Point out each Plasmodium parasite.
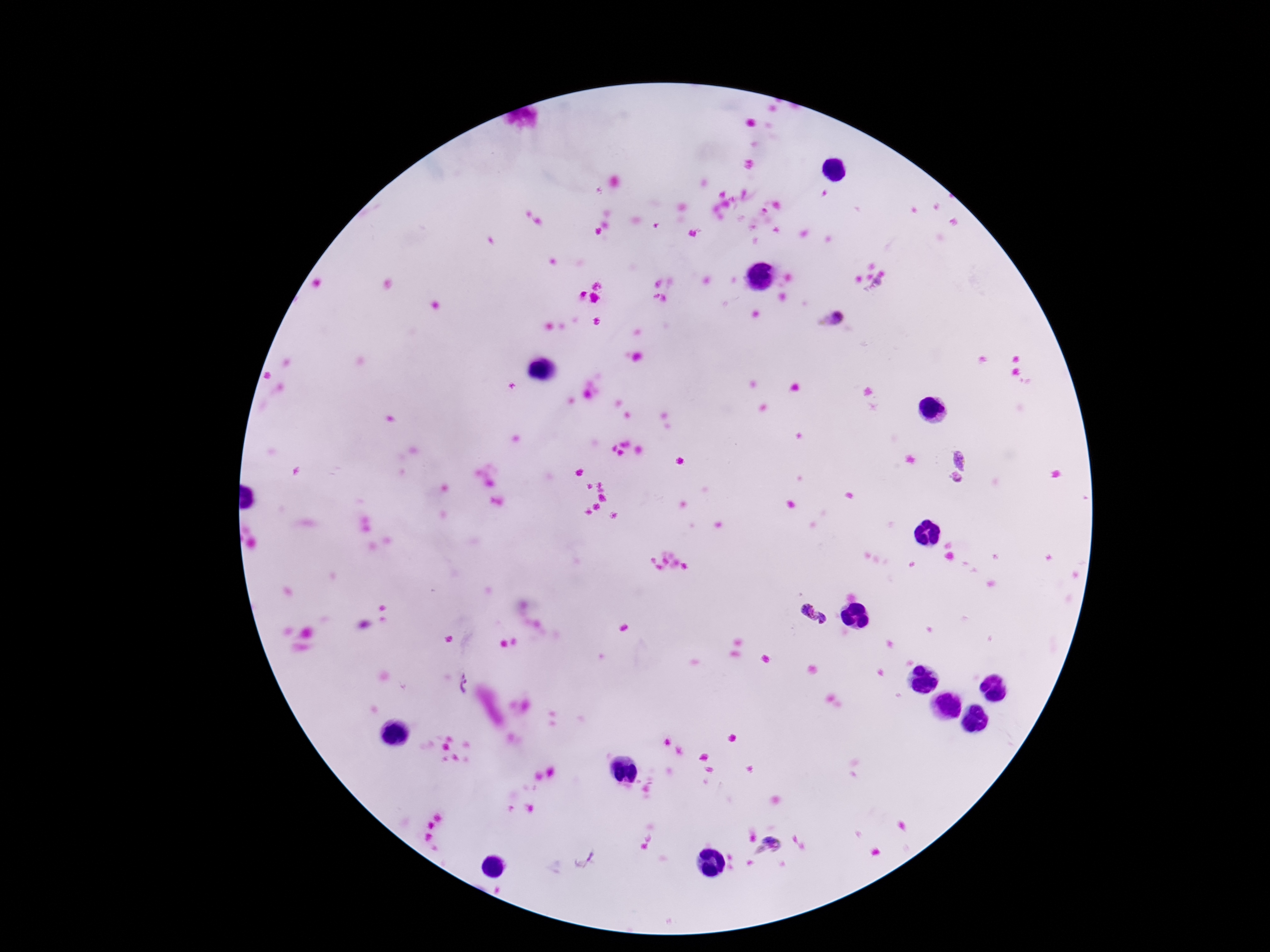
Approximate centers as {x, y} in pixels.
Plasmodium parasites: {832, 319}, {958, 459}, {954, 479}, {814, 615}, {461, 685}, {774, 841}, {583, 859}.

stain: Giemsa
patient_malaria_status: positive
image_size: 1270×952 pixels
field_of_view: one from this slide
magnification: 100x
capture: smartphone camera through the microscope eyepiece
preparation: thick peripheral-blood smear